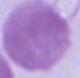
magnification: 1000x
identification: erythrocyte
modality: micrograph